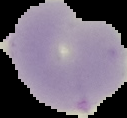

image size = 127×118 pixels
image type = segmented cell region on a black background
malaria status = uninfected
preparation = thin blood film